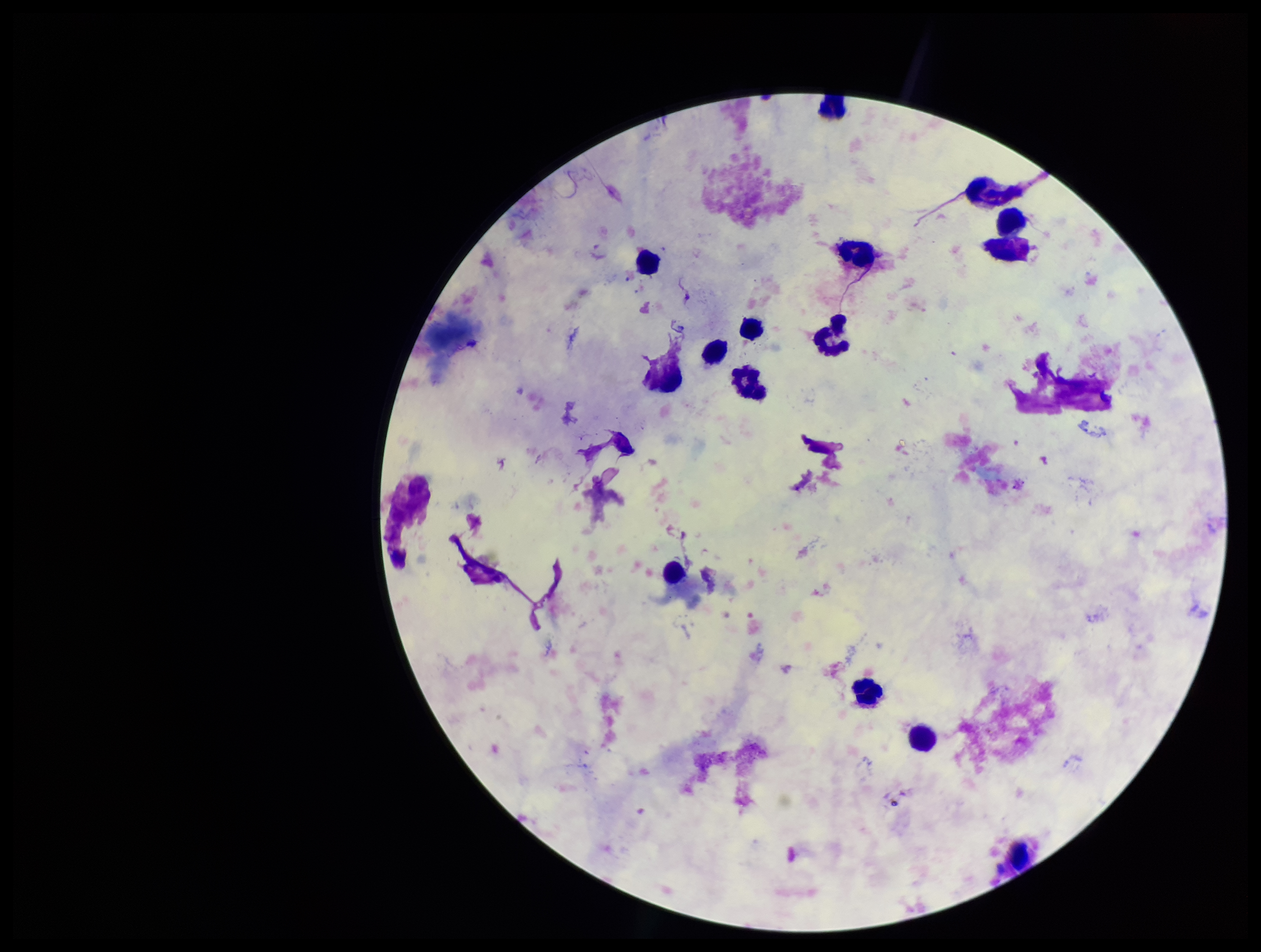
image size = 1261×952 pixels
capture = smartphone photograph through the microscope eyepiece
stain = Giemsa
Plasmodium parasites = none seen
parasite count = 0
patient malaria status = negative
leukocyte count = 14
field of view = single
preparation = thick blood smear